State which parasite is depicted.
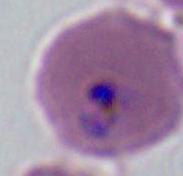

This is Plasmodium.

magnification = 400x or 1000x
modality = photomicrograph